Name the cell type shown.
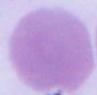

An erythrocyte.

{
  "magnification": "1000x",
  "modality": "photomicrograph"
}